Mark where platelets are.
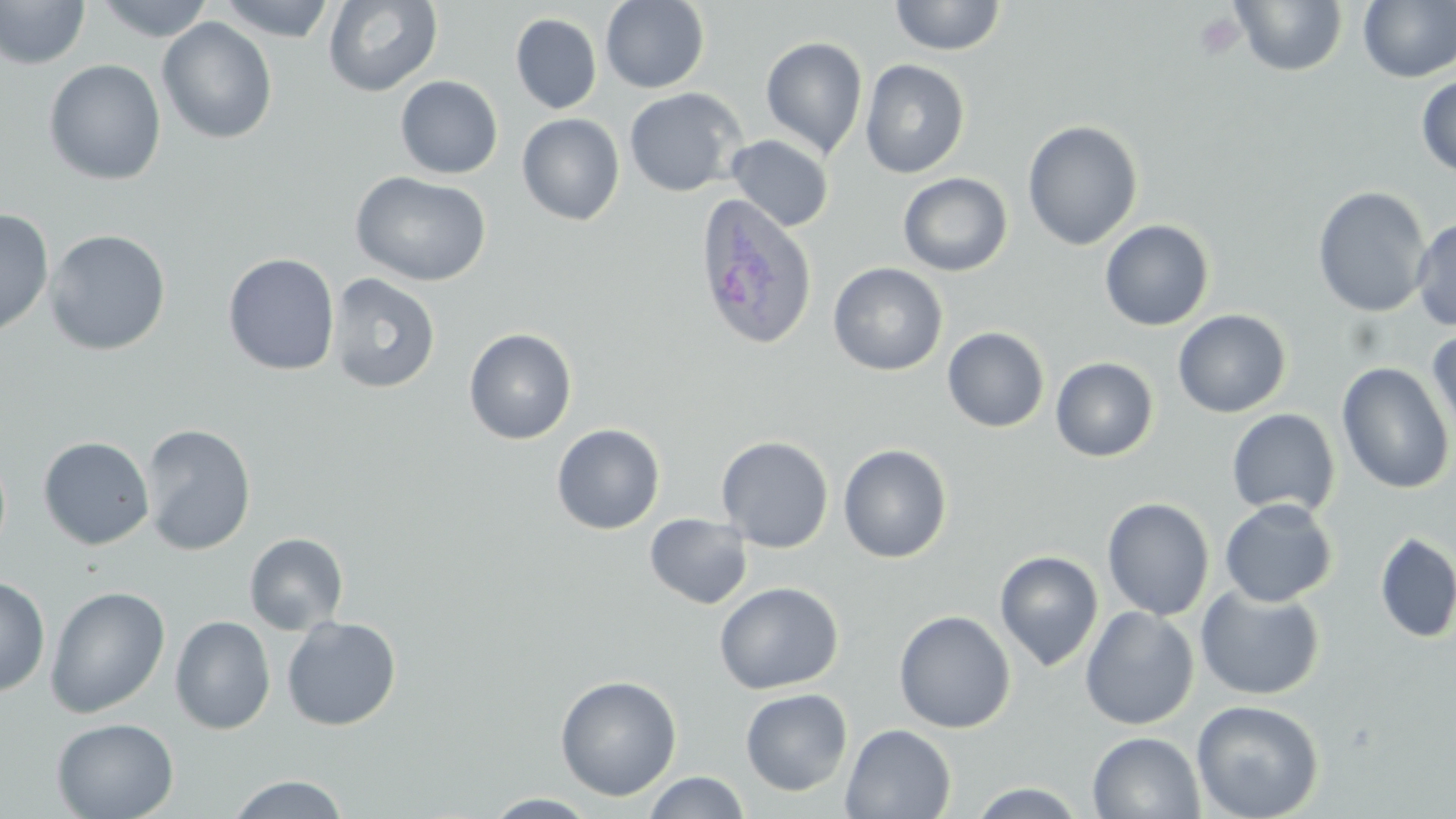

Approximate bounding boxes as (x1, y1, x2, y2) in pixels.
Platelets: (1194, 11, 1244, 60).

Plasmodium ovale-infected red blood cell locations: (693, 193, 818, 352). Uninfected red blood cell locations: (94, 0, 214, 42), (217, 0, 336, 42), (322, 0, 443, 97), (600, 0, 710, 93), (889, 0, 1006, 56), (1230, 0, 1348, 76), (0, 1, 91, 69), (1358, 1, 1456, 83), (511, 13, 602, 114), (157, 17, 278, 145), (760, 36, 868, 159), (44, 59, 167, 185), (859, 59, 970, 179), (395, 75, 503, 179), (1416, 75, 1456, 178), (624, 87, 747, 197), (516, 113, 625, 226), (1022, 120, 1144, 250), (726, 134, 834, 232), (350, 171, 493, 286), (898, 172, 1013, 277), (1312, 185, 1432, 318), (0, 209, 55, 338), (1411, 216, 1456, 331), (1099, 220, 1214, 331), (44, 229, 171, 356), (223, 253, 340, 376), (827, 262, 948, 376), (327, 273, 441, 394), (1173, 309, 1291, 417), (942, 326, 1050, 432), (463, 328, 577, 445), (1427, 330, 1456, 447), (1050, 357, 1159, 462), (1336, 362, 1455, 494), (1226, 408, 1341, 518), (141, 423, 256, 555), (551, 423, 665, 535), (716, 435, 835, 553), (38, 436, 155, 551), (838, 443, 953, 563), (1102, 497, 1215, 620), (1219, 498, 1338, 607), (644, 513, 753, 610), (244, 532, 349, 635), (1374, 532, 1456, 644), (995, 550, 1104, 671), (0, 574, 51, 697), (714, 581, 844, 695), (45, 585, 171, 718), (1195, 585, 1326, 701), (1080, 605, 1199, 730), (894, 609, 1016, 734), (170, 615, 276, 735), (282, 616, 402, 731), (554, 674, 682, 801), (740, 687, 853, 796), (1191, 699, 1325, 819), (51, 717, 179, 819), (841, 723, 956, 818), (1088, 731, 1205, 819), (642, 771, 750, 818), (227, 774, 350, 818), (966, 781, 1091, 817), (483, 792, 600, 818). Slide-level diagnosis: Plasmodium ovale. Captured at 1000x magnification. Light microscopy. One field of a larger specimen. Image is 1456×819 pixels. Thin blood film. May-Grünwald-Giemsa stain.